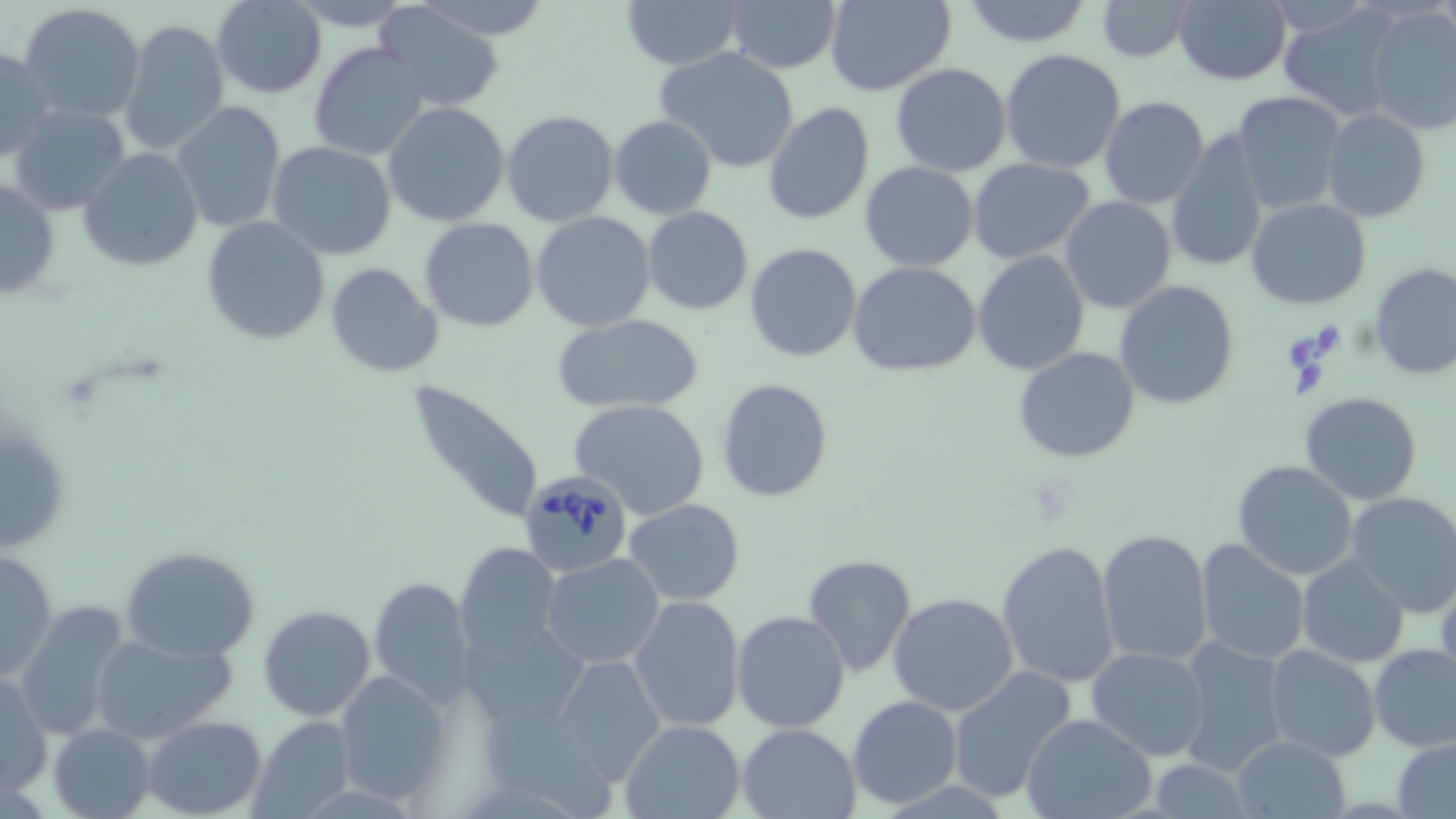

Summary:
  - Coordinate format: approximate bounding boxes as [x1, y1, x2, y2] in pixels
  - Babesia divergens-infected red blood cell locations: [519, 472, 633, 576]
  - Uninfected red blood cell locations: [210, 0, 327, 99], [286, 0, 414, 31], [414, 0, 554, 41], [723, 0, 842, 73], [957, 0, 1096, 48], [1096, 0, 1196, 62], [1172, 0, 1292, 85], [622, 1, 745, 70], [821, 1, 957, 95], [19, 2, 146, 122], [372, 3, 507, 113], [1274, 3, 1400, 120], [1365, 6, 1456, 135], [120, 19, 230, 158], [308, 41, 432, 163], [1, 45, 55, 162], [654, 47, 804, 174], [999, 48, 1127, 172], [889, 62, 1013, 176], [1231, 92, 1347, 215], [1098, 97, 1210, 209], [172, 101, 285, 232], [383, 101, 509, 226], [762, 102, 876, 226], [6, 104, 132, 217], [1321, 108, 1430, 223], [500, 109, 619, 228], [609, 115, 717, 220], [1165, 134, 1269, 274], [267, 142, 398, 261], [78, 148, 204, 271], [969, 159, 1096, 263], [860, 161, 979, 271], [0, 173, 59, 304], [1060, 196, 1176, 313], [1246, 198, 1370, 310], [642, 207, 753, 314], [532, 211, 655, 330], [201, 216, 330, 344], [420, 218, 539, 331], [744, 242, 862, 361], [972, 251, 1089, 375], [849, 261, 982, 378], [325, 262, 444, 379], [1368, 264, 1456, 380], [1115, 279, 1239, 411], [550, 313, 705, 415], [1013, 346, 1142, 463], [409, 379, 547, 528], [716, 379, 833, 501], [1300, 391, 1423, 504], [571, 399, 711, 520], [0, 430, 69, 550], [1232, 460, 1360, 581], [1208, 483, 1329, 630], [1343, 492, 1456, 616], [624, 498, 744, 605], [1097, 528, 1214, 667], [996, 537, 1121, 688], [1194, 538, 1309, 665], [455, 542, 563, 661], [119, 543, 263, 662], [2, 545, 58, 685], [540, 553, 666, 670], [801, 555, 919, 678], [1297, 555, 1409, 669], [367, 577, 475, 704], [889, 593, 1019, 715], [627, 594, 744, 731], [14, 602, 132, 740], [257, 603, 376, 721], [732, 610, 850, 733], [90, 631, 235, 744], [1174, 637, 1291, 777], [1369, 643, 1456, 751], [1264, 644, 1381, 763], [1087, 646, 1211, 760], [550, 653, 664, 786], [947, 666, 1078, 805], [334, 669, 453, 807], [0, 675, 51, 797], [848, 694, 963, 808], [1020, 713, 1155, 819], [144, 715, 267, 818], [248, 715, 355, 817], [620, 718, 746, 818], [735, 722, 861, 818], [48, 723, 155, 819], [1231, 733, 1350, 816], [1393, 736, 1456, 818]
  - Slide-level diagnosis: Babesia divergens
  - Modality: optical microscopy
  - Field of view: one of a larger specimen
  - Image size: 1456×819 pixels
  - Preparation: thin blood film
  - Magnification: 1000x
  - Stain: May-Grünwald-Giemsa